Locate every blood parasite and identify its species.
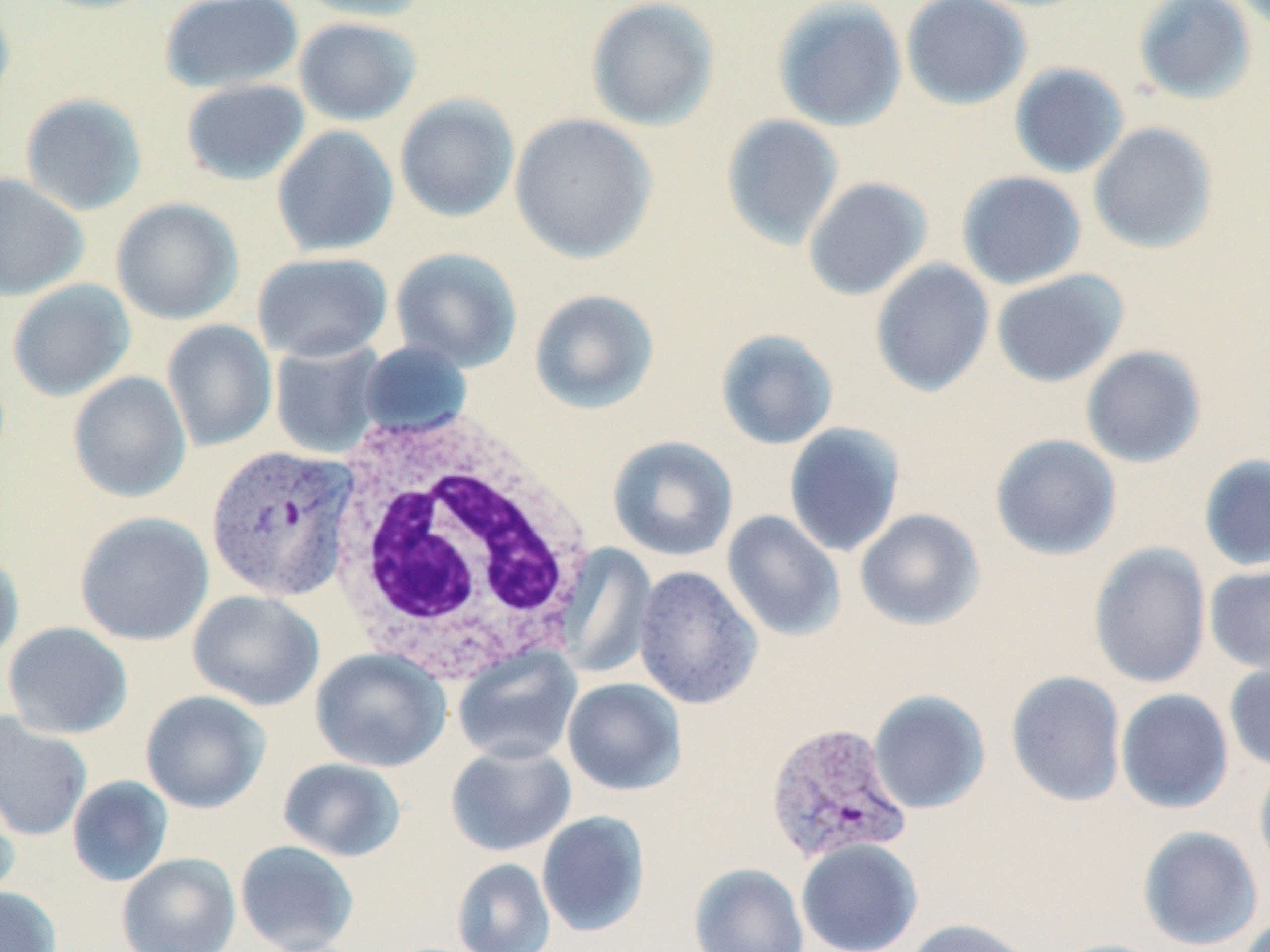

Approximate bounding boxes as (x1, y1, x2, y2) in pixels.
Plasmodium vivax-infected red blood cells: (207, 443, 361, 602), (764, 721, 913, 865).
No Plasmodium falciparum, Plasmodium ovale, Plasmodium malariae, Babesia divergens, or Trypanosoma brucei observed.

White blood cell locations: (321, 405, 595, 676). Uninfected red blood cell locations: (0, 0, 16, 119), (159, 0, 304, 93), (294, 0, 431, 22), (585, 0, 720, 131), (901, 0, 1032, 110), (1132, 0, 1258, 105), (772, 1, 907, 132), (293, 17, 421, 126), (1008, 63, 1129, 178), (180, 78, 310, 186), (19, 93, 148, 216), (394, 93, 521, 223), (509, 113, 657, 263), (721, 114, 844, 249), (1088, 122, 1219, 254), (271, 125, 399, 258), (956, 170, 1087, 290), (0, 173, 89, 301), (802, 177, 933, 300), (111, 197, 244, 325), (390, 247, 522, 372), (252, 252, 393, 362), (870, 259, 995, 397), (990, 270, 1128, 387), (7, 279, 136, 401), (529, 289, 660, 414), (162, 320, 277, 452), (715, 329, 839, 450), (270, 340, 386, 459), (358, 340, 472, 439), (1080, 345, 1206, 468), (67, 371, 192, 503), (783, 422, 905, 557), (990, 434, 1122, 560), (607, 436, 738, 562), (1199, 454, 1270, 572), (854, 508, 985, 631), (721, 510, 845, 642), (74, 511, 214, 646), (1088, 542, 1211, 689), (557, 543, 658, 679), (0, 550, 24, 667), (633, 565, 762, 709), (1204, 565, 1270, 675), (187, 589, 325, 711), (2, 622, 133, 740), (452, 645, 583, 765), (310, 648, 451, 772), (1224, 660, 1270, 771), (1005, 671, 1126, 807), (562, 678, 687, 795), (1115, 688, 1234, 813), (140, 690, 270, 814), (867, 690, 991, 815), (0, 712, 93, 841), (445, 742, 576, 856), (278, 757, 407, 862), (1253, 757, 1270, 884), (67, 776, 174, 887), (0, 781, 20, 904), (536, 810, 651, 937), (1137, 825, 1263, 951), (796, 838, 923, 952), (235, 840, 359, 952), (117, 853, 241, 952), (452, 858, 555, 952), (688, 862, 810, 952), (0, 887, 61, 952), (1236, 912, 1270, 952), (903, 918, 1039, 952), (1047, 938, 1171, 952). Slide-level diagnosis: Plasmodium vivax. Image is 1270×952 pixels. May-Grünwald-Giemsa stain. Light microscopy. Single field of view. 1000x magnification. Thin blood smear.